Outline each blood parasite and name the species.
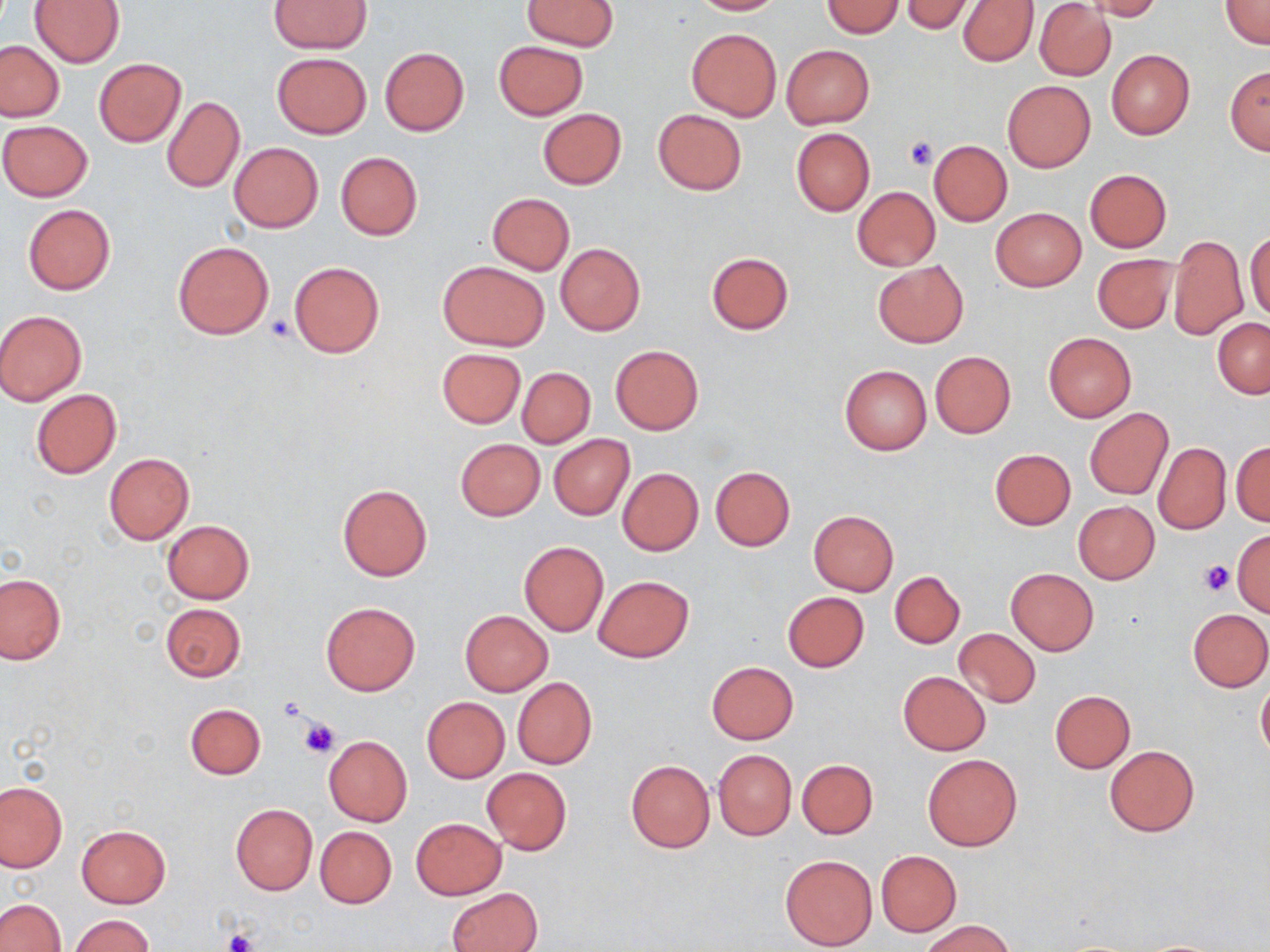

No blood parasites observed.

slide-level diagnosis = negative for blood parasites
preparation = thin blood film
modality = light microscopy
magnification = 1000x
image size = 1270×952 pixels
uninfected red blood cell locations = approximate bounding boxes as (x1, y1, x2, y2) in pixels: (30, 0, 125, 67), (690, 0, 783, 15), (958, 0, 1037, 66), (1080, 0, 1164, 20), (1220, 0, 1268, 48), (268, 1, 370, 52), (520, 1, 619, 51), (822, 1, 902, 38), (900, 1, 976, 34), (1034, 2, 1116, 81), (687, 28, 781, 121), (495, 40, 587, 119), (0, 41, 64, 122), (781, 45, 875, 128), (379, 48, 469, 135), (1106, 49, 1194, 138), (272, 52, 371, 138), (94, 58, 185, 147), (1225, 66, 1270, 154), (1002, 80, 1094, 171), (161, 96, 245, 192), (537, 108, 627, 189), (653, 108, 747, 196), (0, 120, 93, 200), (791, 128, 875, 216), (929, 140, 1012, 226), (228, 142, 323, 232), (336, 151, 423, 241), (1084, 169, 1171, 253), (853, 186, 939, 271), (487, 193, 575, 273), (23, 204, 114, 295), (990, 207, 1086, 291), (1246, 232, 1270, 323), (1168, 235, 1249, 339), (172, 240, 274, 339), (556, 244, 645, 335), (705, 251, 794, 334), (1092, 253, 1176, 333), (438, 260, 549, 351), (290, 261, 384, 358), (873, 261, 968, 348), (0, 308, 87, 405), (1213, 318, 1270, 398), (1043, 333, 1136, 421), (609, 344, 703, 434), (436, 347, 525, 428), (930, 351, 1015, 438), (440, 359, 592, 437), (839, 365, 932, 454), (517, 367, 595, 448), (30, 388, 121, 479), (1085, 407, 1174, 500), (548, 435, 634, 519), (455, 439, 545, 520), (1231, 440, 1269, 527), (1154, 442, 1231, 535), (990, 448, 1076, 530), (103, 453, 194, 544), (709, 466, 795, 551), (618, 468, 704, 555), (337, 484, 432, 581), (1073, 501, 1158, 584), (809, 510, 898, 595), (162, 521, 254, 603), (1232, 529, 1270, 619), (519, 541, 609, 637), (1005, 568, 1098, 656), (889, 570, 964, 648), (0, 573, 65, 665), (592, 576, 694, 662), (782, 591, 870, 672), (321, 601, 420, 696), (160, 603, 246, 682), (1188, 609, 1270, 691), (460, 610, 552, 695), (953, 628, 1041, 706), (706, 661, 798, 743), (897, 671, 990, 755), (512, 677, 597, 770), (1256, 680, 1270, 760), (1050, 690, 1135, 772), (421, 696, 509, 782), (185, 703, 265, 778), (323, 735, 412, 826), (1104, 746, 1200, 836), (713, 749, 796, 840), (922, 753, 1022, 851), (626, 759, 714, 852), (797, 759, 878, 838), (482, 767, 572, 854), (0, 782, 66, 872), (230, 804, 317, 895), (412, 818, 505, 899), (76, 825, 170, 909), (314, 826, 397, 908), (876, 850, 962, 937), (780, 853, 877, 950), (449, 887, 542, 952), (0, 898, 67, 952), (70, 915, 153, 952), (924, 920, 1011, 952)
platelet locations = approximate bounding boxes as (x1, y1, x2, y2) in pixels: (904, 137, 937, 169), (1200, 560, 1235, 595), (296, 714, 341, 756), (223, 931, 257, 952)
stain = May-Grünwald-Giemsa
field of view = single